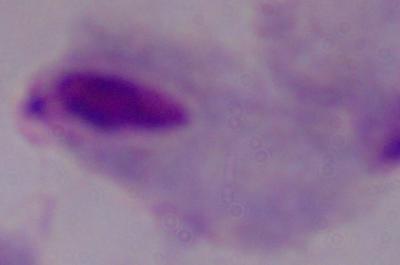
Captured at 1000x magnification. Photomicrograph. A trichomonad is seen.